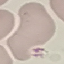
malaria status = uninfected
capture = smartphone camera at the microscope eyepiece
image type = cell patch, automatically extracted from a larger field of view and resized to 64 × 64 pixels
stain = Giemsa
preparation = thin blood smear